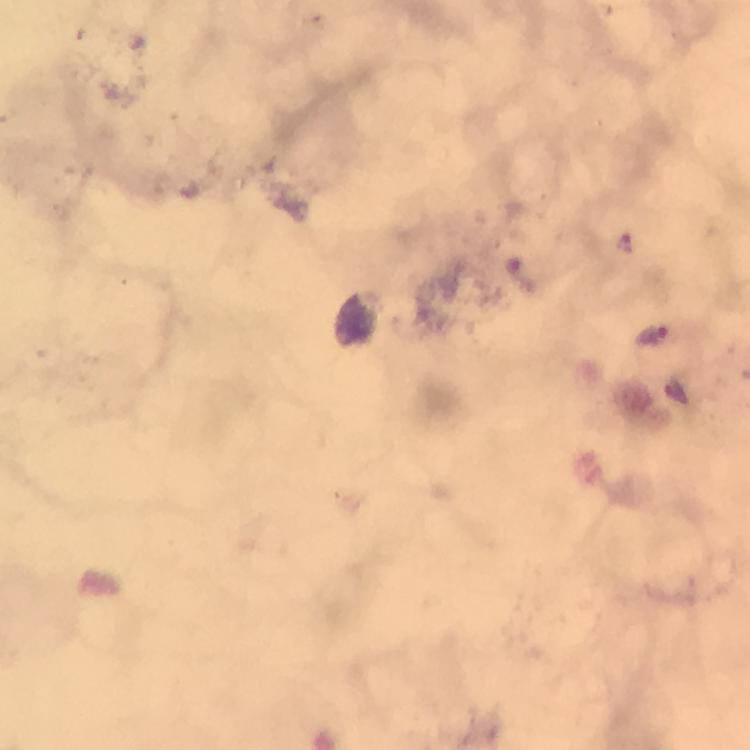
Approximate centers as {x, y} in pixels. Malaria parasite locations: {624, 241}, {652, 335}. Cropped region of a single field of view. 100x magnification. From a malaria diagnostic workup. Smartphone photograph taken through a microscope. Image is 750×750 pixels. Giemsa stain. Immersion oil applied. Thick blood smear.